Point out every Plasmodium parasite and every leukocyte.
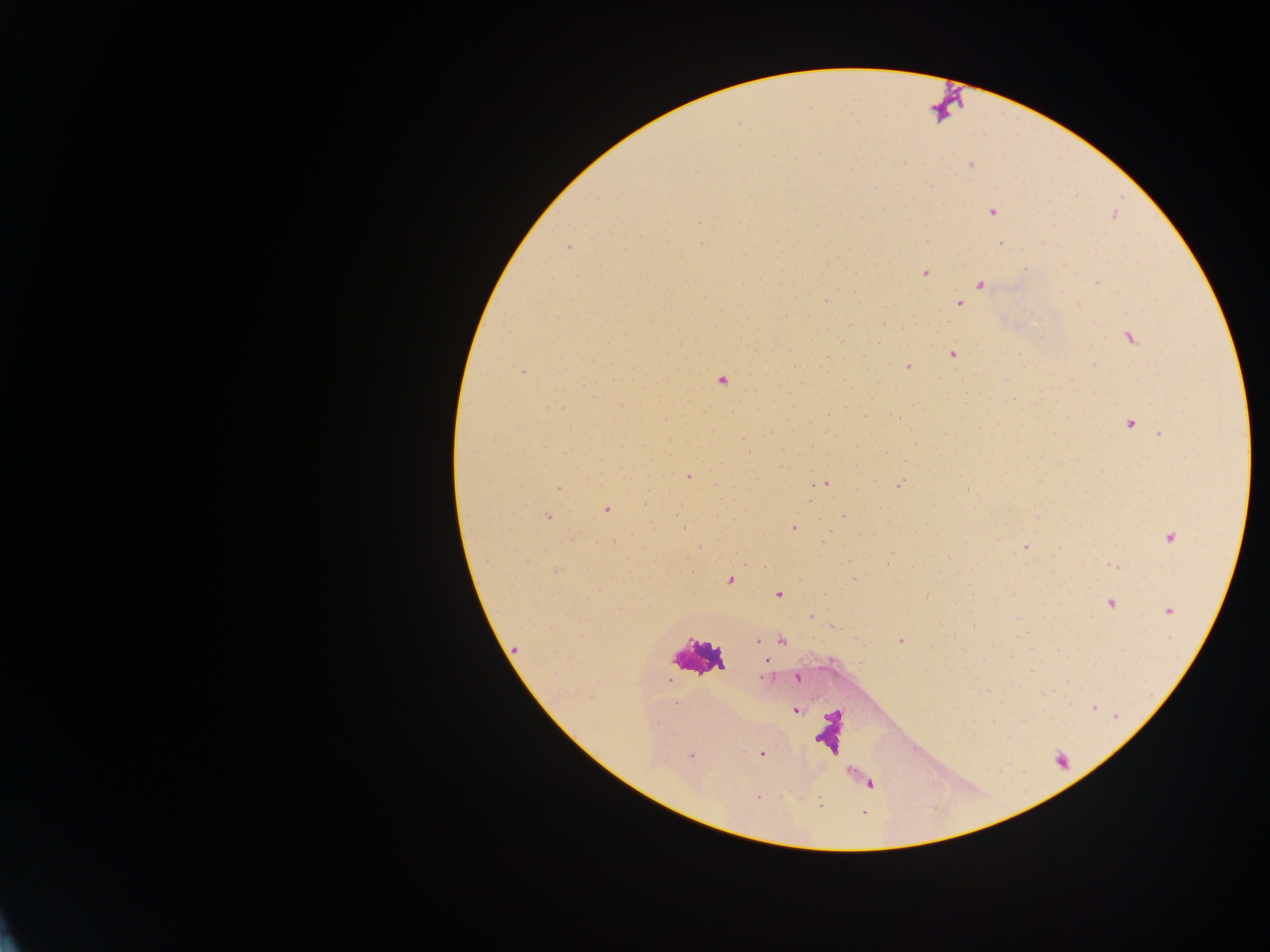
Approximate centers as x y in pixels.
Plasmodium parasites: 970 165; 993 211; 699 223; 1001 243; 702 244; 568 246; 925 273; 1098 282; 981 284; 705 296; 825 300; 960 305; 721 310; 1131 338; 952 354; 908 367; 523 371; 722 381; 828 415; 898 418; 1130 424; 1161 435; 688 476; 827 484; 901 484; 558 489; 811 501; 605 510; 843 516; 547 517; 793 528; 1170 538; 613 543; 1026 547; 887 564; 1112 566; 730 580; 778 595; 927 596; 1110 603; 1169 611; 811 616; 782 640; 758 641; 901 641; 516 648; 766 659; 764 678; 797 678; 675 704; 796 711; 657 723; 762 754; 691 755.
Leukocytes: 699 657.

field of view = single
image size = 1270×952 pixels
capture = mobile-phone photograph through a microscope
preparation = thick blood smear
country = Ghana